Outline each blood parasite and name the species.
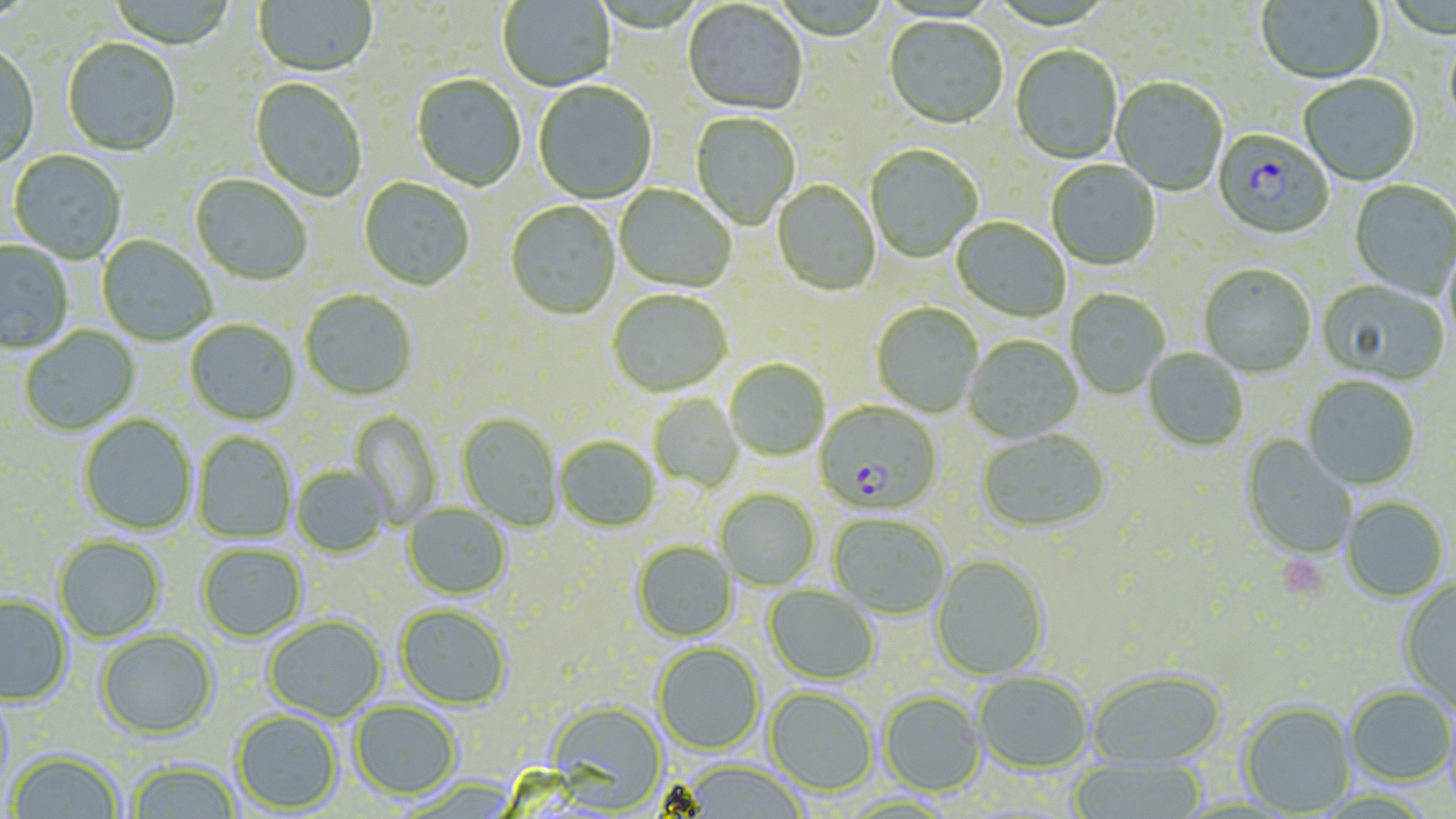
Approximate bounding boxes as [x1, y1, x2, y2] in pixels.
Plasmodium falciparum-infected red blood cells: [1212, 130, 1334, 240], [815, 401, 943, 514].
No Plasmodium ovale, Plasmodium malariae, Plasmodium vivax, Babesia divergens, or Trypanosoma brucei observed.

Uninfected red blood cell locations: [108, 0, 236, 51], [253, 0, 378, 78], [497, 0, 616, 92], [1256, 0, 1385, 86], [682, 2, 807, 117], [883, 17, 1007, 131], [1443, 29, 1456, 138], [62, 39, 181, 157], [0, 45, 40, 170], [1011, 46, 1123, 165], [412, 75, 527, 192], [1298, 76, 1421, 187], [1111, 78, 1228, 197], [250, 79, 367, 202], [533, 82, 657, 204], [690, 113, 801, 230], [866, 146, 983, 264], [9, 150, 126, 263], [1046, 161, 1161, 272], [190, 175, 313, 286], [358, 177, 475, 291], [1349, 180, 1456, 300], [772, 181, 880, 297], [614, 185, 736, 292], [505, 202, 621, 320], [951, 218, 1070, 323], [97, 235, 217, 346], [1443, 236, 1456, 355], [0, 240, 73, 354], [1199, 265, 1316, 379], [1317, 280, 1450, 387], [1065, 288, 1170, 399], [300, 289, 418, 400], [607, 290, 732, 397], [872, 303, 983, 418], [186, 320, 300, 425], [19, 326, 139, 436], [964, 335, 1083, 443], [1143, 349, 1248, 453], [725, 358, 830, 461], [1302, 378, 1420, 491], [649, 393, 744, 492], [350, 411, 443, 528], [457, 413, 562, 532], [79, 415, 197, 534], [976, 429, 1110, 535], [193, 431, 297, 543], [1241, 435, 1357, 560], [555, 436, 661, 532], [291, 466, 391, 557], [716, 489, 820, 590], [1341, 497, 1448, 602], [403, 503, 511, 599], [828, 513, 950, 619], [54, 535, 165, 642], [632, 541, 737, 641], [196, 543, 307, 641], [930, 554, 1050, 680], [1399, 578, 1456, 712], [763, 585, 881, 685], [0, 596, 72, 706], [396, 605, 512, 709], [263, 616, 386, 722], [96, 629, 219, 740], [653, 642, 764, 754], [1087, 669, 1226, 770], [973, 672, 1092, 773], [764, 687, 877, 795], [1345, 687, 1455, 785], [879, 691, 986, 796], [350, 701, 461, 799], [547, 701, 668, 812], [1239, 701, 1355, 816], [232, 711, 342, 814], [8, 751, 124, 818], [127, 760, 242, 819], [1068, 760, 1206, 819], [679, 761, 807, 818]. Platelet locations: [1276, 555, 1331, 600]. Slide-level diagnosis: Plasmodium falciparum. One field of a larger specimen. Thin blood film. May-Grünwald-Giemsa stain. Image is 1456×819 pixels. Light microscopy. 1000x magnification.